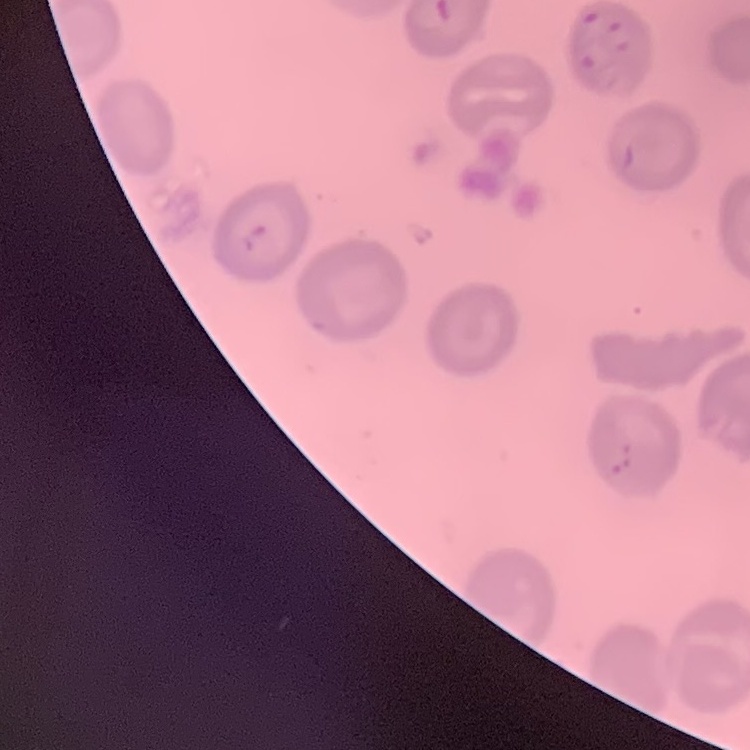
The erythrocytes show no rouleaux formation. One tile cut from a larger photomicrograph. Thin blood film. Stained with either Field's or Giemsa.